Assess the morphology of the erythrocytes.
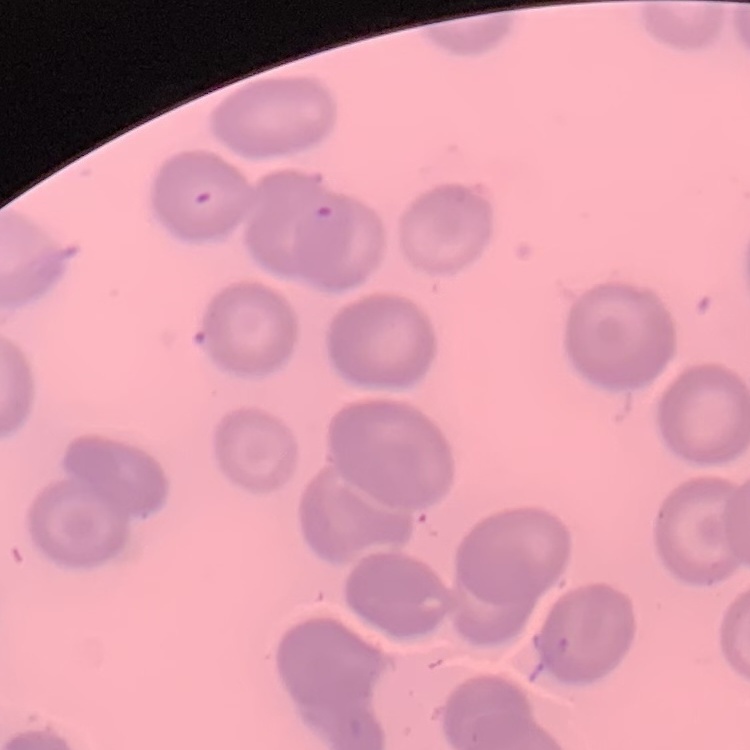

They show no rouleaux formation.

image type = square crop of a larger photomicrograph
preparation = thin blood film
stain = Field's or Giemsa